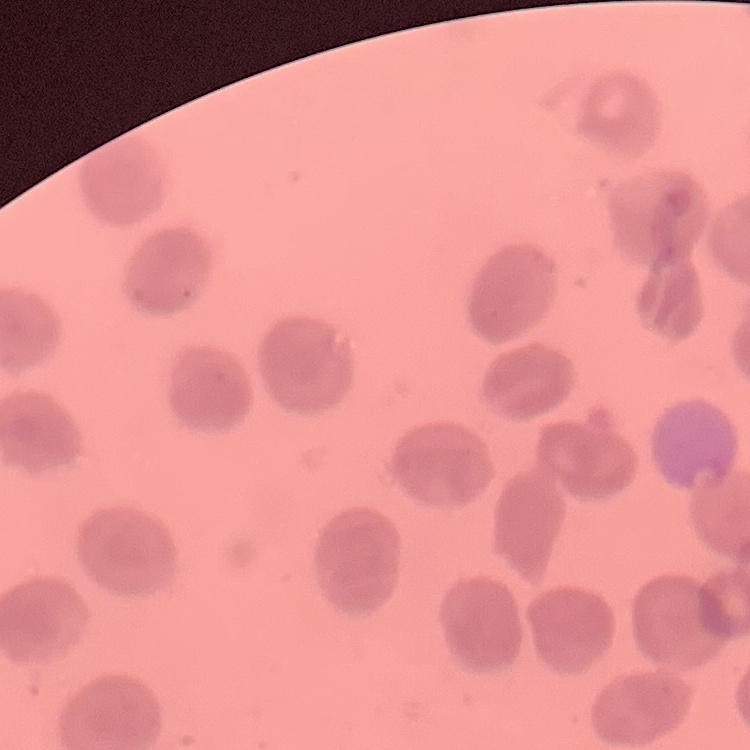
red_blood_cell_morphology: no rouleaux formation
stain: Field's or Giemsa
image_type: one tile cut from a larger photomicrograph
preparation: thin blood smear